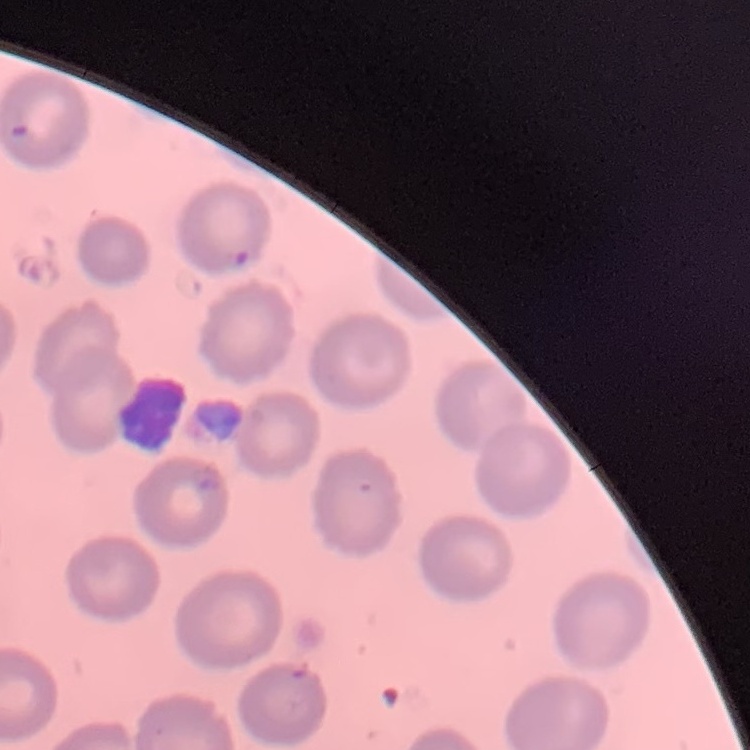

erythrocyte morphology = no rouleaux formation
preparation = thin blood smear
stain = Field's or Giemsa
image type = one tile cut from a larger photomicrograph